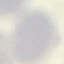
Summary:
  - Malaria status: uninfected
  - Stain: Giemsa
  - Capture: smartphone through the microscope eyepiece
  - Preparation: thin blood smear
  - Image type: cell patch, automatically extracted from a larger field of view and resized to 64 × 64 pixels